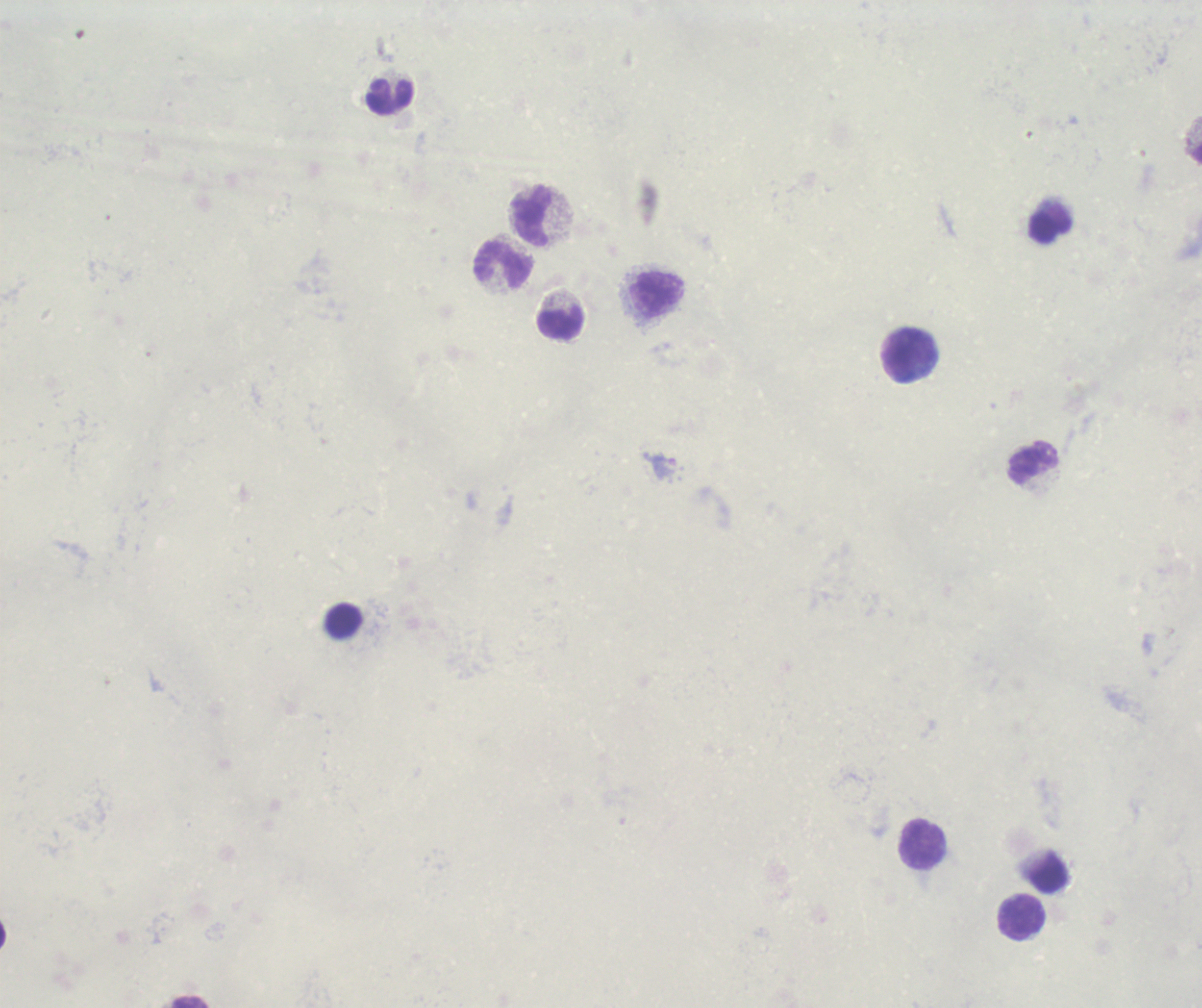
Approximate centers as {x, y} in pixels. Leukocyte locations: {390, 97}, {532, 217}, {1050, 228}, {504, 266}, {657, 295}, {560, 323}, {909, 356}, {1034, 463}, {923, 844}, {1024, 918}. Image is 1202×1008 pixels. Previously used in an actual diagnosis. Result: no Plasmodium parasites seen. Background quality: unsatisfactory. Thick blood smear. Single field of view. 100x magnification. Romanowsky-stained preparation.